Report the malaria status of this cell.
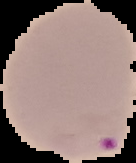

It is parasitized.

{
  "image_type": "cell region segmented out of the field of view; surrounding area masked to black",
  "image_size": "136×163 pixels",
  "preparation": "thin blood film"
}